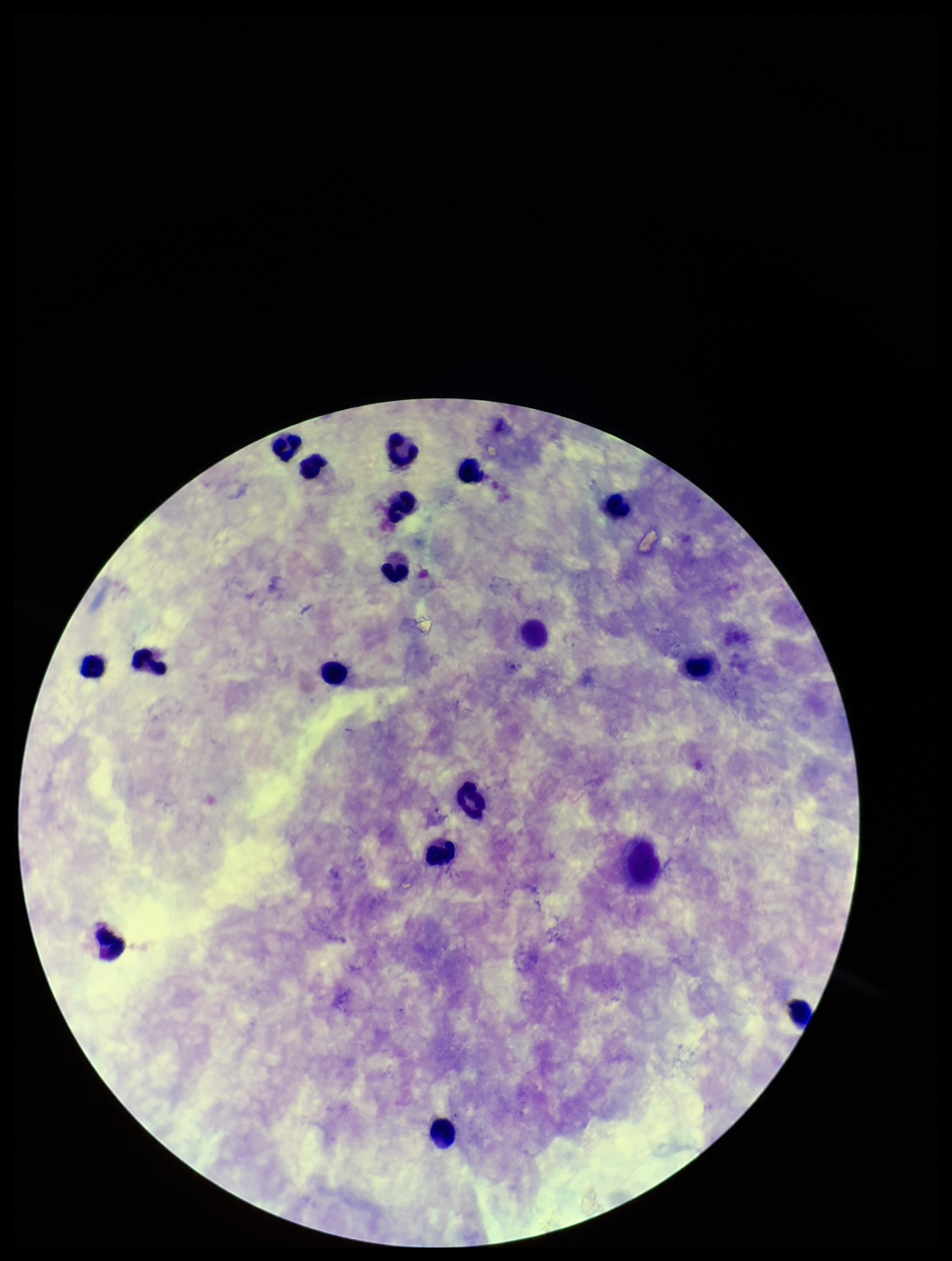

Summary:
  - Parasite count: 0
  - Field of view: one from this slide
  - Image size: 952×1261 pixels
  - Leukocyte count: 16
  - Capture: smartphone photograph through the microscope eyepiece
  - Plasmodium parasites: none seen
  - Preparation: thick blood smear
  - Stain: Giemsa
  - Patient malaria status: negative